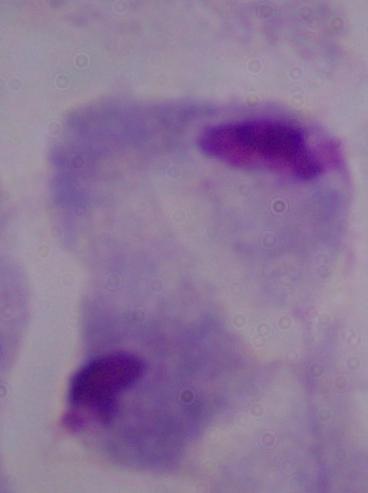

identification: trichomonad
magnification: 1000x
modality: photomicrograph